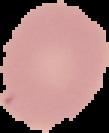 Cell region segmented out of the field of view; the surrounding area is masked to black. From a thin blood smear. Image is 109×133 pixels. Malaria status: uninfected.